Assess the morphology of the erythrocytes.
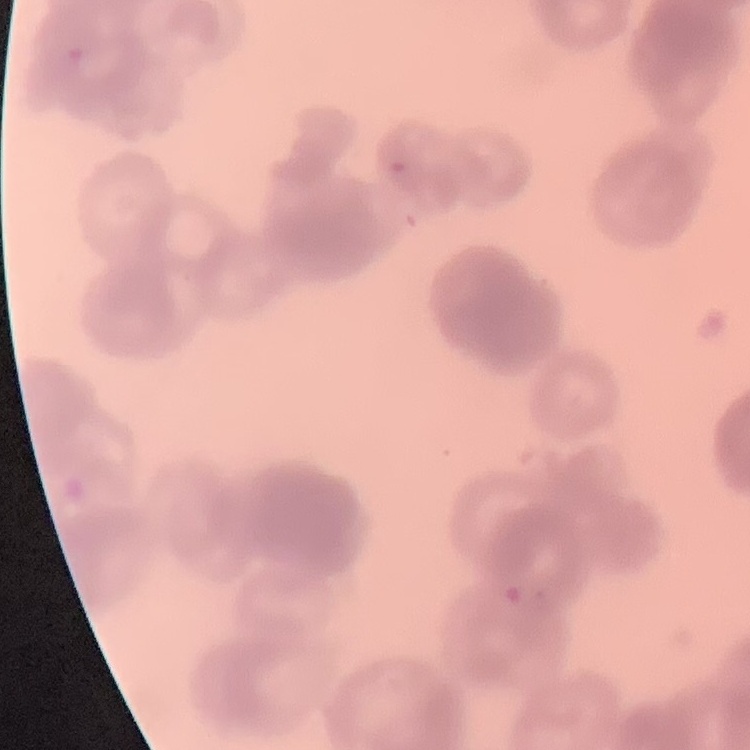

Rouleaux formation.

Thin peripheral smear. Square crop of a larger photomicrograph. Stained with either Field's or Giemsa.